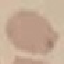

Summary:
  - Result: negative for malaria parasites
  - Image type: cell patch, automatically extracted from a larger field of view and resized to 64 × 64 pixels
  - Preparation: thin blood smear
  - Capture: smartphone through the microscope eyepiece
  - Stain: Giemsa